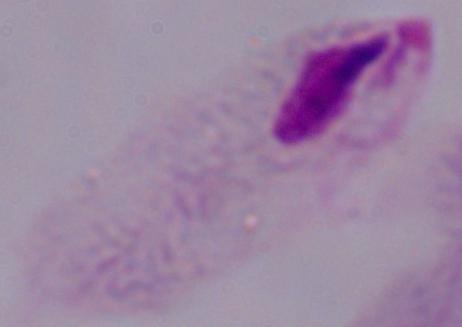
identification = trichomonad
magnification = 1000x
modality = micrograph